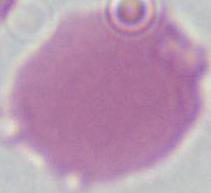

Summary:
  - Magnification: 1000x
  - Modality: micrograph
  - Identification: erythrocyte